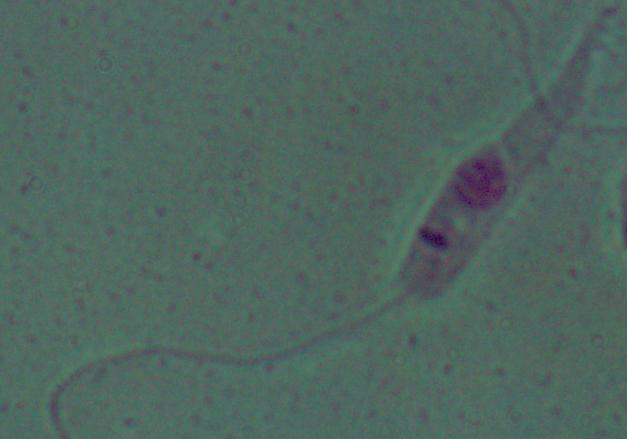
Summary:
  - Modality: micrograph
  - Magnification: 1000x
  - Identification: Leishmania